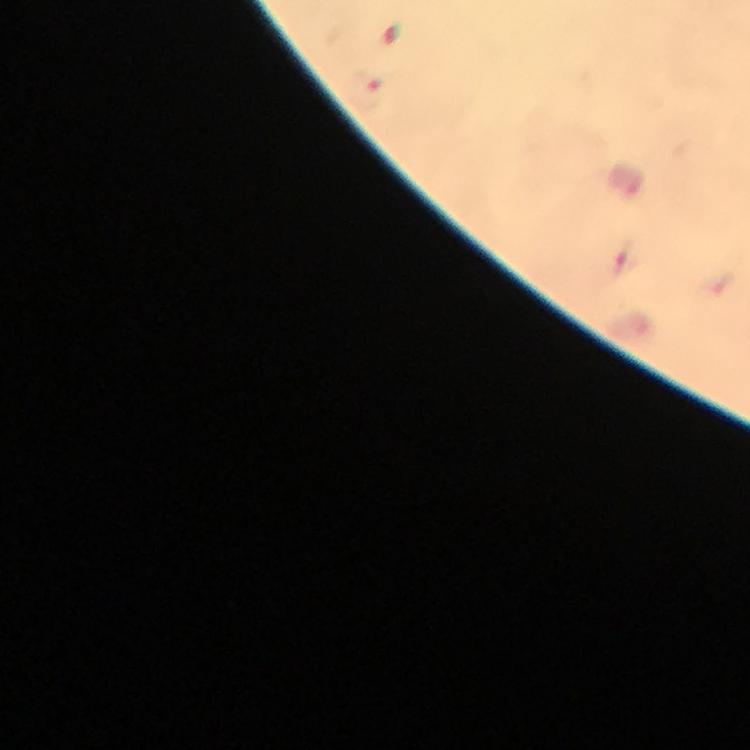
Approximate centers as (x, y) in pixels.
Summary:
  - Plasmodium parasite locations: (622, 260)
  - Magnification: 100x
  - Capture: smartphone camera through the microscope
  - Image size: 750×750 pixels
  - Stain: Giemsa
  - Context: from a malaria diagnostic workup
  - Cropped from: a single field of view
  - Preparation: thick blood film
  - Immersion oil: used